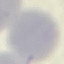
result = no malaria parasites detected
image type = automatically extracted cell patch, resized to 64 × 64 pixels
preparation = thin smear
stain = Giemsa
capture = smartphone camera at the microscope eyepiece